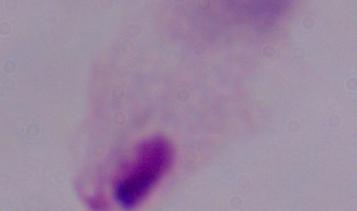
magnification: 1000x
identification: trichomonad
modality: photomicrograph